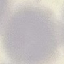
result = no malaria parasites seen
image type = cell patch, automatically extracted from a larger field of view and resized to 64 × 64 pixels
preparation = thin blood film
capture = smartphone through the microscope eyepiece
stain = Giemsa